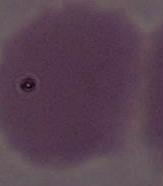
Summary:
  - Identification: red blood cell
  - Modality: micrograph
  - Magnification: 1000x